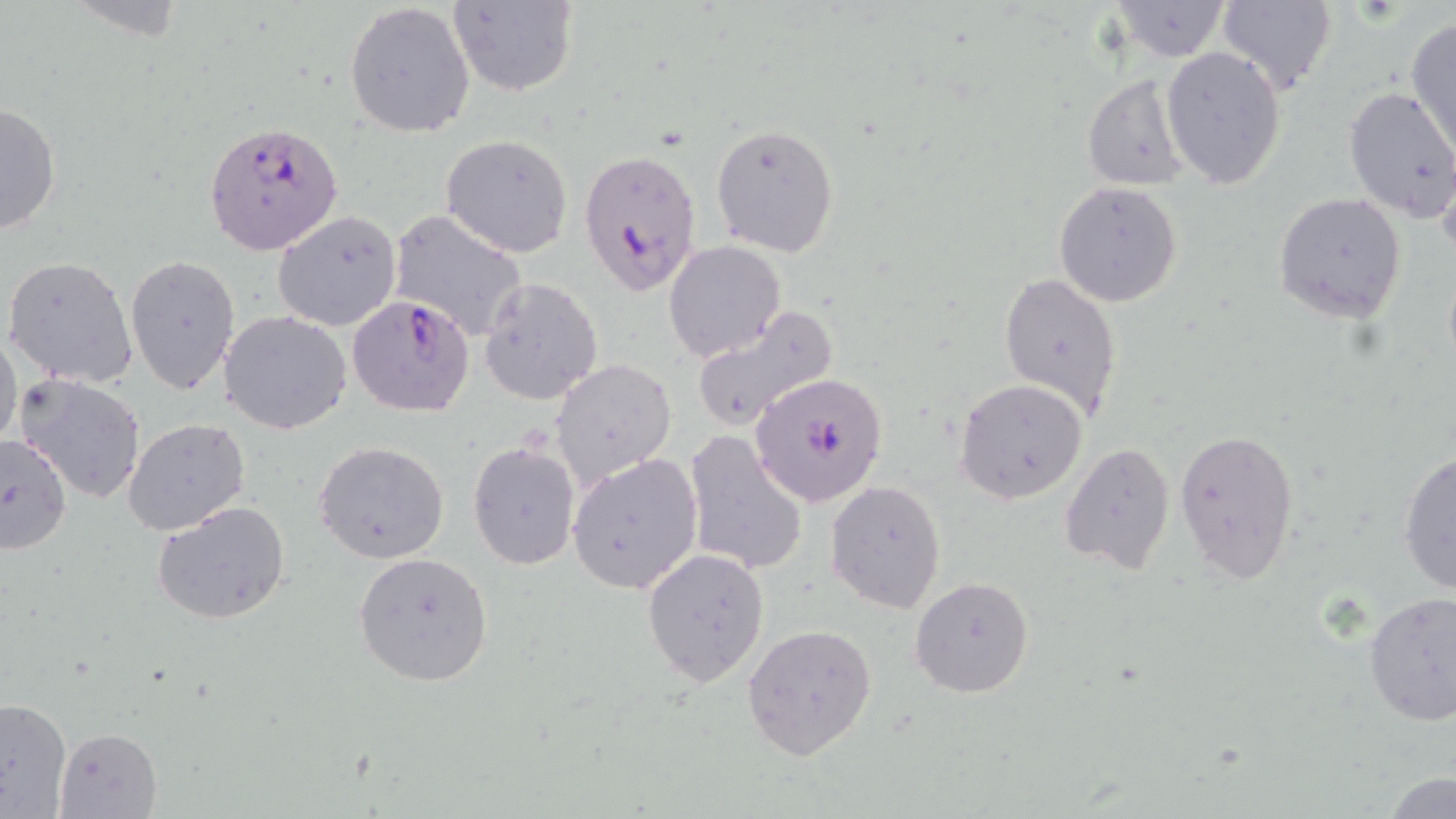

Approximate bounding boxes as named x1/y1/x2/y2 corners in pixels. Uninfected red blood cell locations: (x1=1217, y1=0, x2=1339, y2=96), (x1=447, y1=1, x2=580, y2=97), (x1=344, y1=2, x2=475, y2=137), (x1=1108, y1=2, x2=1234, y2=62), (x1=1405, y1=16, x2=1456, y2=158), (x1=1161, y1=47, x2=1287, y2=190), (x1=1080, y1=74, x2=1192, y2=191), (x1=1343, y1=86, x2=1456, y2=221), (x1=1, y1=99, x2=63, y2=238), (x1=709, y1=123, x2=840, y2=258), (x1=441, y1=134, x2=573, y2=258), (x1=1052, y1=181, x2=1183, y2=307), (x1=1273, y1=192, x2=1407, y2=323), (x1=386, y1=209, x2=531, y2=341), (x1=272, y1=210, x2=404, y2=331), (x1=663, y1=241, x2=786, y2=362), (x1=126, y1=254, x2=241, y2=398), (x1=3, y1=255, x2=138, y2=389), (x1=999, y1=271, x2=1124, y2=422), (x1=478, y1=276, x2=603, y2=405), (x1=691, y1=305, x2=838, y2=431), (x1=218, y1=309, x2=352, y2=435), (x1=1, y1=325, x2=21, y2=456), (x1=549, y1=358, x2=677, y2=488), (x1=16, y1=372, x2=147, y2=504), (x1=955, y1=378, x2=1089, y2=505), (x1=123, y1=417, x2=250, y2=537), (x1=1173, y1=426, x2=1300, y2=586), (x1=683, y1=429, x2=809, y2=577), (x1=0, y1=434, x2=72, y2=556), (x1=314, y1=441, x2=450, y2=564), (x1=468, y1=441, x2=580, y2=570), (x1=1059, y1=441, x2=1176, y2=574), (x1=1397, y1=449, x2=1456, y2=598), (x1=568, y1=454, x2=703, y2=595), (x1=825, y1=479, x2=946, y2=613), (x1=152, y1=500, x2=293, y2=625), (x1=641, y1=547, x2=769, y2=689), (x1=352, y1=550, x2=495, y2=686), (x1=909, y1=577, x2=1033, y2=698), (x1=1363, y1=592, x2=1456, y2=726), (x1=742, y1=621, x2=878, y2=759), (x1=0, y1=697, x2=72, y2=817), (x1=55, y1=725, x2=162, y2=819), (x1=1381, y1=771, x2=1456, y2=819). Plasmodium falciparum-infected red blood cell locations: (x1=204, y1=120, x2=346, y2=255), (x1=577, y1=147, x2=705, y2=296), (x1=347, y1=295, x2=476, y2=416), (x1=748, y1=372, x2=889, y2=507). Slide-level diagnosis: Plasmodium falciparum. 1000x magnification. Single field of view. Thin blood smear. May-Grünwald-Giemsa-stained preparation. Optical microscopy. Image is 1456×819 pixels.